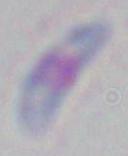 1000x magnification. Photomicrograph. Toxoplasma gondii is shown.